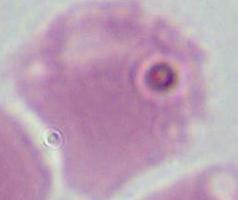

An erythrocyte is shown. Micrograph. 1000x magnification.